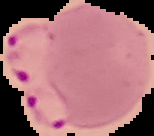

Summary:
  - Image type: segmented cell region on a black background
  - Malaria status: parasitized
  - Preparation: thin blood film
  - Image size: 154×136 pixels